Classify this cell by malaria status.
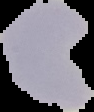
It is uninfected.

Summary:
  - Image type: segmented cell region on a black background
  - Image size: 94×112 pixels
  - Preparation: thin blood smear